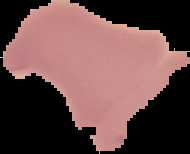
image size = 190×154 pixels
preparation = thin blood smear
image type = segmented cell region on a black background
result = no malaria parasites seen